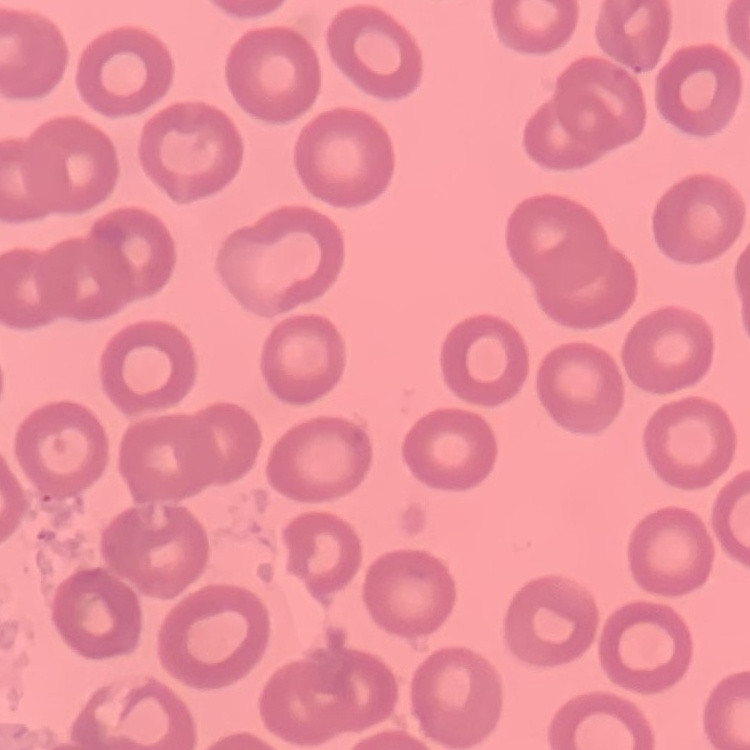

Summary:
  - Erythrocyte morphology: no rouleaux formation
  - Stain: Field's or Giemsa
  - Preparation: thin blood film
  - Image type: one tile cut from a larger photomicrograph